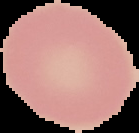
preparation = thin blood smear
image size = 139×133 pixels
image type = segmented cell region on a black background
result = negative for malaria parasites